Assess this cell for malaria.
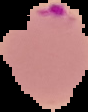

It is parasitized.

Summary:
  - Image size: 88×112 pixels
  - Preparation: thin blood film
  - Image type: segmented cell region with the area outside set to black